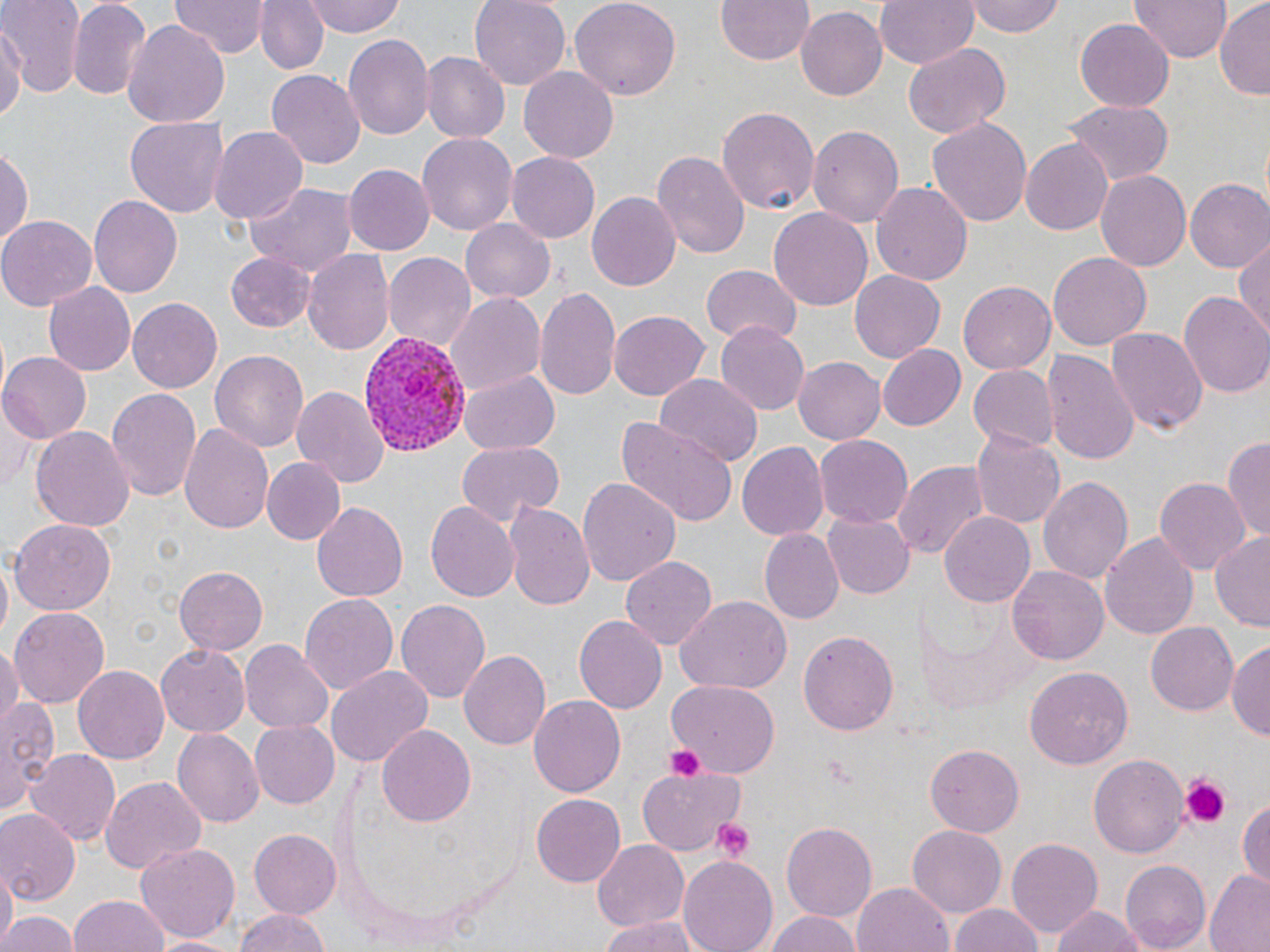

Approximate bounding boxes as [x1, y1, x2, y2] in pixels. Uninfected red blood cell locations: [0, 0, 84, 94], [65, 0, 150, 101], [171, 0, 266, 58], [256, 0, 328, 75], [309, 0, 407, 38], [470, 0, 569, 89], [570, 0, 680, 99], [711, 0, 813, 67], [875, 0, 979, 72], [966, 0, 1065, 39], [1131, 1, 1229, 62], [1213, 2, 1270, 99], [798, 5, 888, 103], [0, 17, 24, 129], [1075, 19, 1174, 112], [122, 20, 229, 128], [342, 34, 434, 144], [902, 43, 1009, 140], [422, 51, 510, 143], [518, 67, 619, 163], [264, 70, 366, 170], [1064, 101, 1173, 189], [716, 104, 820, 214], [928, 117, 1032, 231], [126, 118, 228, 218], [807, 125, 905, 229], [210, 126, 308, 224], [419, 133, 517, 238], [1021, 136, 1114, 237], [1, 148, 33, 249], [652, 149, 748, 261], [507, 152, 599, 243], [343, 164, 433, 255], [1095, 170, 1191, 272], [1184, 179, 1270, 275], [870, 180, 973, 288], [244, 182, 356, 276], [586, 191, 681, 291], [88, 196, 182, 302], [769, 206, 873, 311], [0, 215, 96, 310], [459, 216, 555, 306], [1233, 236, 1270, 340], [303, 245, 395, 354], [1047, 249, 1151, 348], [225, 251, 316, 334], [382, 253, 475, 349], [703, 264, 802, 346], [851, 269, 945, 361], [42, 281, 136, 378], [958, 281, 1055, 375], [535, 286, 622, 405], [1181, 291, 1270, 402], [448, 293, 545, 397], [127, 297, 223, 393], [610, 311, 708, 400], [716, 324, 809, 415], [1108, 327, 1207, 438], [877, 343, 967, 431], [1044, 349, 1139, 468], [209, 350, 309, 452], [1, 352, 89, 441], [794, 355, 885, 444], [967, 365, 1057, 450], [457, 369, 560, 452], [654, 375, 762, 470], [103, 385, 200, 501], [293, 385, 389, 489], [2, 400, 37, 493], [613, 418, 737, 529], [178, 420, 274, 534], [31, 426, 134, 533], [970, 428, 1065, 525], [816, 434, 913, 527], [1225, 436, 1270, 542], [455, 440, 566, 527], [737, 441, 830, 541], [263, 459, 345, 545], [895, 459, 990, 558], [576, 475, 680, 587], [1039, 475, 1134, 584], [1153, 476, 1250, 573], [502, 501, 594, 610], [311, 502, 407, 604], [425, 502, 518, 603], [942, 512, 1033, 606], [822, 514, 912, 599], [9, 518, 117, 615], [759, 529, 844, 626], [1099, 530, 1200, 642], [1211, 531, 1270, 631], [619, 555, 718, 652], [172, 564, 268, 657], [1007, 564, 1108, 668], [298, 592, 401, 697], [675, 594, 792, 695], [395, 599, 492, 705], [8, 606, 110, 709], [575, 614, 668, 712], [1147, 622, 1240, 714], [799, 628, 899, 734], [239, 640, 333, 733], [1229, 640, 1270, 745], [0, 644, 19, 727], [157, 645, 249, 736], [458, 650, 549, 749], [72, 663, 168, 761], [326, 666, 434, 769], [1025, 667, 1133, 770], [666, 680, 781, 774], [528, 693, 626, 798], [0, 695, 58, 807], [248, 719, 337, 808], [171, 724, 262, 824], [376, 726, 474, 827], [923, 742, 1025, 837], [26, 750, 119, 847], [1088, 754, 1188, 860], [638, 764, 742, 855], [100, 775, 207, 874], [531, 791, 626, 885], [1237, 798, 1270, 889], [0, 809, 78, 905], [782, 822, 878, 921], [908, 826, 1007, 919], [248, 829, 340, 919], [1006, 836, 1104, 938], [593, 840, 689, 931], [136, 841, 242, 942], [679, 857, 777, 952], [1120, 859, 1210, 951], [1, 864, 16, 946], [1203, 872, 1270, 952], [853, 881, 954, 952], [69, 895, 168, 952], [948, 904, 1044, 952], [233, 907, 333, 952], [1046, 908, 1145, 952], [1, 909, 78, 952], [764, 911, 859, 952], [599, 916, 702, 952], [151, 933, 243, 951]. Plasmodium vivax-infected red blood cell locations: [358, 332, 469, 456]. Platelet locations: [664, 746, 707, 780], [1177, 774, 1228, 827], [711, 816, 759, 861]. Slide-level diagnosis: Plasmodium vivax. 1000x magnification. Thin blood film. Image is 1270×952 pixels. Light microscopy. May-Grünwald-Giemsa-stained preparation. Single field of view.